Comment on the morphology of the erythrocytes.
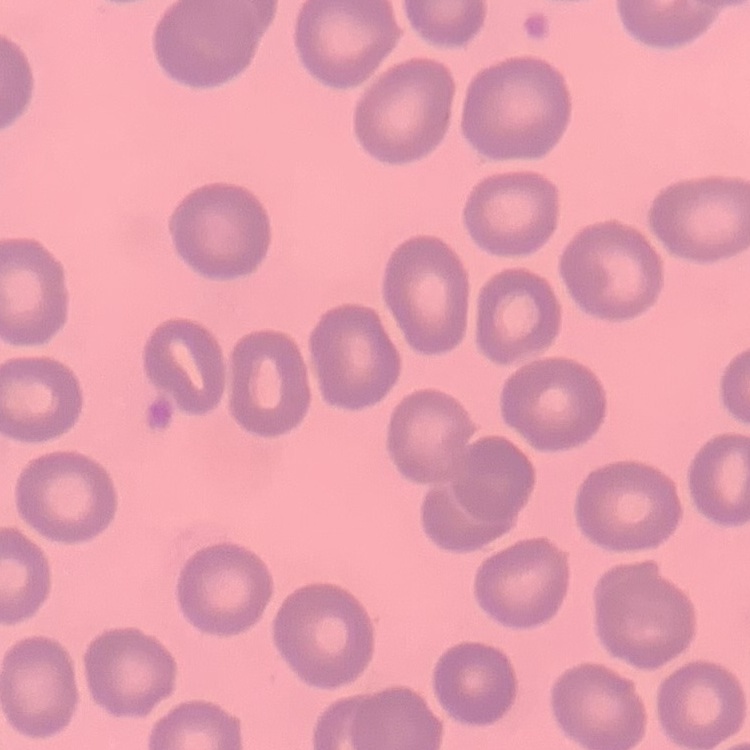

They show no rouleaux formation.

Summary:
  - Stain: Field's or Giemsa
  - Image type: one tile cut from a larger photomicrograph
  - Preparation: thin blood smear